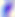

magnification = 400x
modality = photomicrograph
identification = Toxoplasma gondii